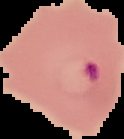
image size = 124×139 pixels
result = Plasmodium parasites detected
image type = cell region segmented out of the field of view; surrounding area masked to black
preparation = thin blood smear